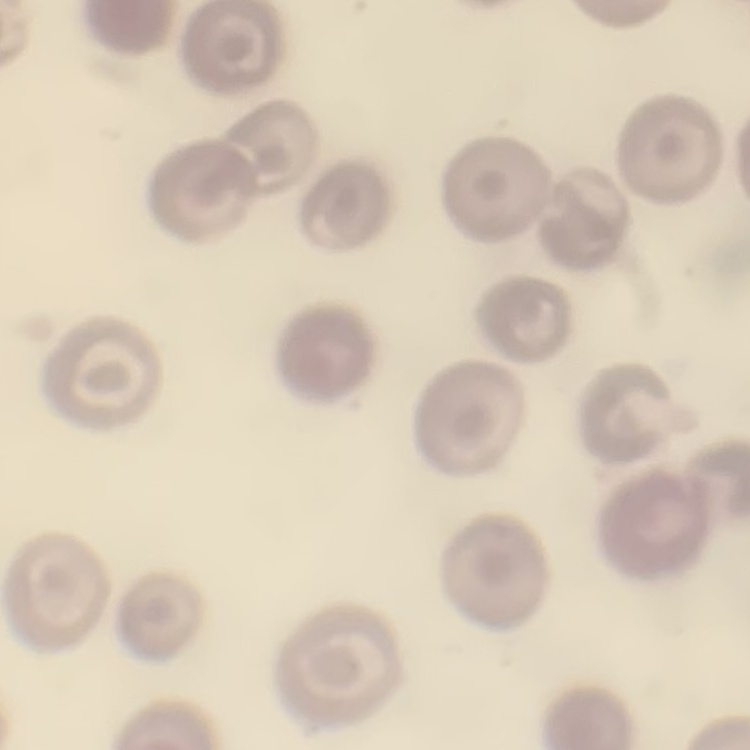

Summary:
  - Erythrocyte morphology: no rouleaux formation
  - Preparation: thin blood film
  - Image type: one tile cut from a larger photomicrograph
  - Stain: Field's or Giemsa